Locate every leukocyte (white blood cell).
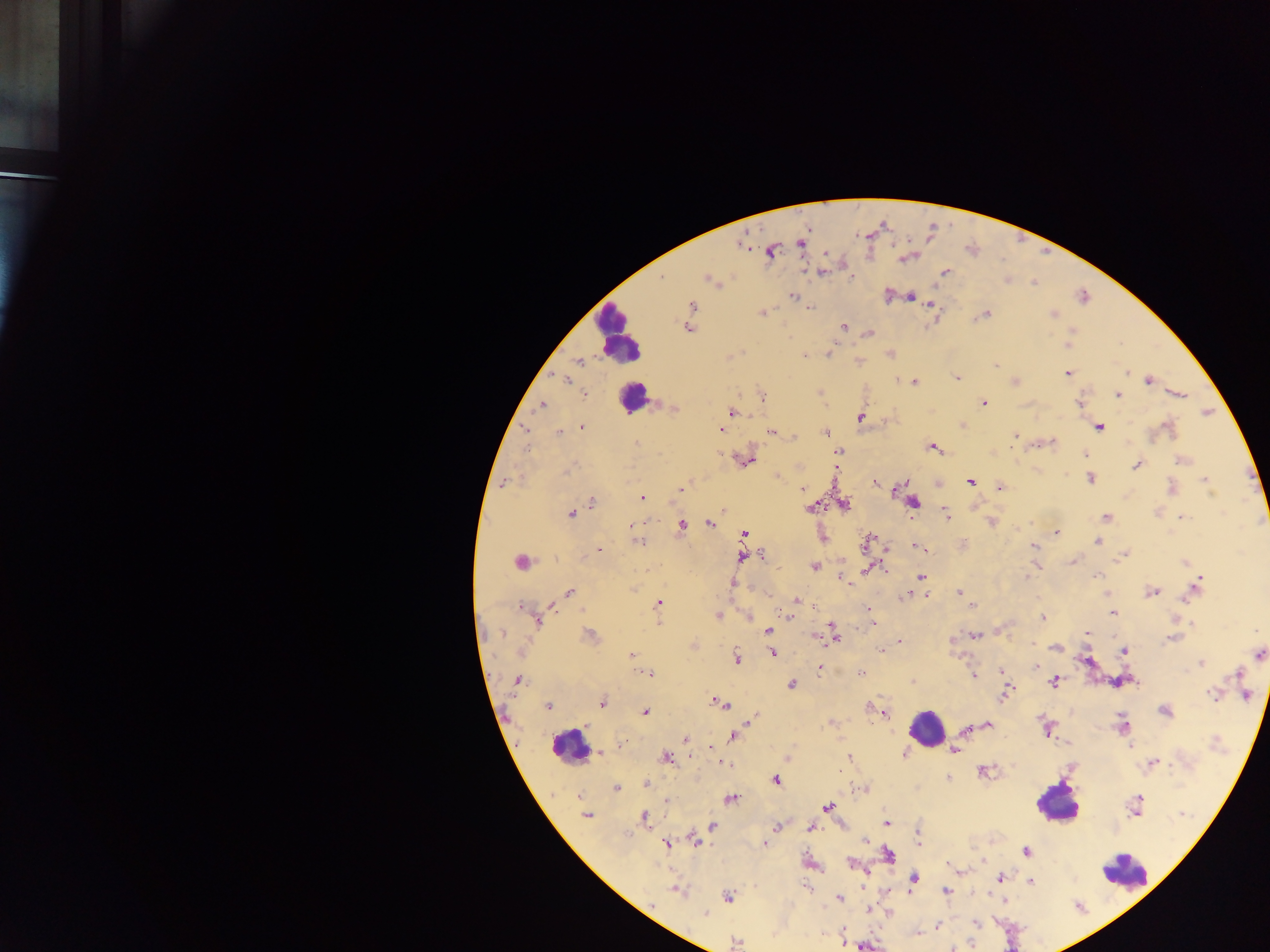
Approximate centers as [x, y] in pixels.
Leukocytes: [618, 331], [633, 398], [926, 727], [569, 747], [1056, 805], [1126, 872].

Summary:
  - Malaria parasite locations: [801, 242], [771, 251], [822, 272], [945, 273], [662, 277], [709, 279], [792, 295], [910, 297], [931, 304], [693, 306], [811, 308], [762, 313], [986, 314], [1053, 315], [843, 326], [686, 328], [870, 333], [1069, 345], [830, 352], [804, 355], [578, 362], [995, 365], [1127, 373], [1067, 374], [957, 378], [1148, 380], [566, 381], [899, 381], [915, 382], [1016, 382], [585, 394], [1179, 394], [1117, 395], [763, 398], [983, 403], [1080, 404], [542, 405], [673, 409], [732, 413], [860, 417], [1099, 427], [1168, 427], [582, 428], [721, 429], [771, 432], [825, 432], [559, 433], [1015, 435], [795, 438], [637, 444], [527, 446], [932, 447], [838, 451], [1085, 454], [747, 460], [1182, 460], [1137, 465], [1090, 478], [1206, 480], [505, 482], [970, 482], [875, 483], [999, 487], [1171, 488], [802, 489], [896, 489], [680, 490], [641, 498], [591, 502], [914, 502], [844, 505], [812, 507], [725, 509], [571, 514], [946, 514], [1106, 517], [1182, 517], [710, 524], [632, 525], [682, 526], [1056, 532], [744, 534], [1097, 541], [638, 542], [866, 543], [1033, 546], [916, 547], [598, 549], [1124, 554], [762, 556], [742, 557], [1073, 561], [520, 562], [1185, 562], [813, 566], [867, 570], [1098, 575], [1027, 576], [921, 577], [842, 579], [846, 582], [733, 583], [1197, 586], [569, 592], [959, 592], [1152, 592], [1191, 594], [906, 595], [797, 600], [659, 603], [972, 606], [520, 607], [552, 608], [868, 608], [782, 611], [787, 613], [1112, 613], [717, 617], [749, 617], [1043, 619], [538, 621], [1192, 622], [659, 623], [874, 624], [768, 631], [1087, 632], [502, 634], [590, 635], [834, 635], [975, 635], [818, 637], [1172, 638], [899, 641], [1034, 644], [1055, 649], [881, 650], [520, 651], [1123, 651], [631, 654], [773, 654], [1258, 654], [736, 658], [1201, 663], [1037, 667], [820, 669], [1001, 670], [860, 673], [649, 674], [974, 675], [1236, 675], [517, 680], [1053, 682], [791, 685], [1212, 694], [1244, 694], [1006, 695], [602, 704], [719, 704], [548, 706], [870, 708], [1165, 711], [646, 712], [883, 713], [757, 717], [1122, 724], [988, 725], [967, 729], [1045, 729], [734, 735], [685, 739], [1131, 746], [711, 747], [955, 750], [600, 753], [904, 753], [665, 758], [849, 758], [1153, 762], [725, 763], [982, 771], [948, 778], [776, 780], [645, 783], [615, 789], [578, 796], [1138, 798], [731, 799], [667, 802], [828, 808], [1182, 814], [586, 815], [645, 816], [886, 823], [713, 826], [777, 827], [811, 827], [917, 836], [696, 840], [865, 840], [667, 843], [764, 844], [1026, 851], [888, 854], [850, 862], [999, 878], [914, 879], [1030, 882], [807, 888], [677, 890], [946, 891], [727, 897], [840, 898], [1004, 901], [869, 908], [705, 913], [976, 923], [938, 926], [843, 933], [917, 935], [736, 942], [865, 946], [954, 948]
  - Field of view: single
  - Image size: 1270×952 pixels
  - Preparation: thick blood smear
  - Capture: mobile-phone photograph through a microscope
  - Country: Ghana